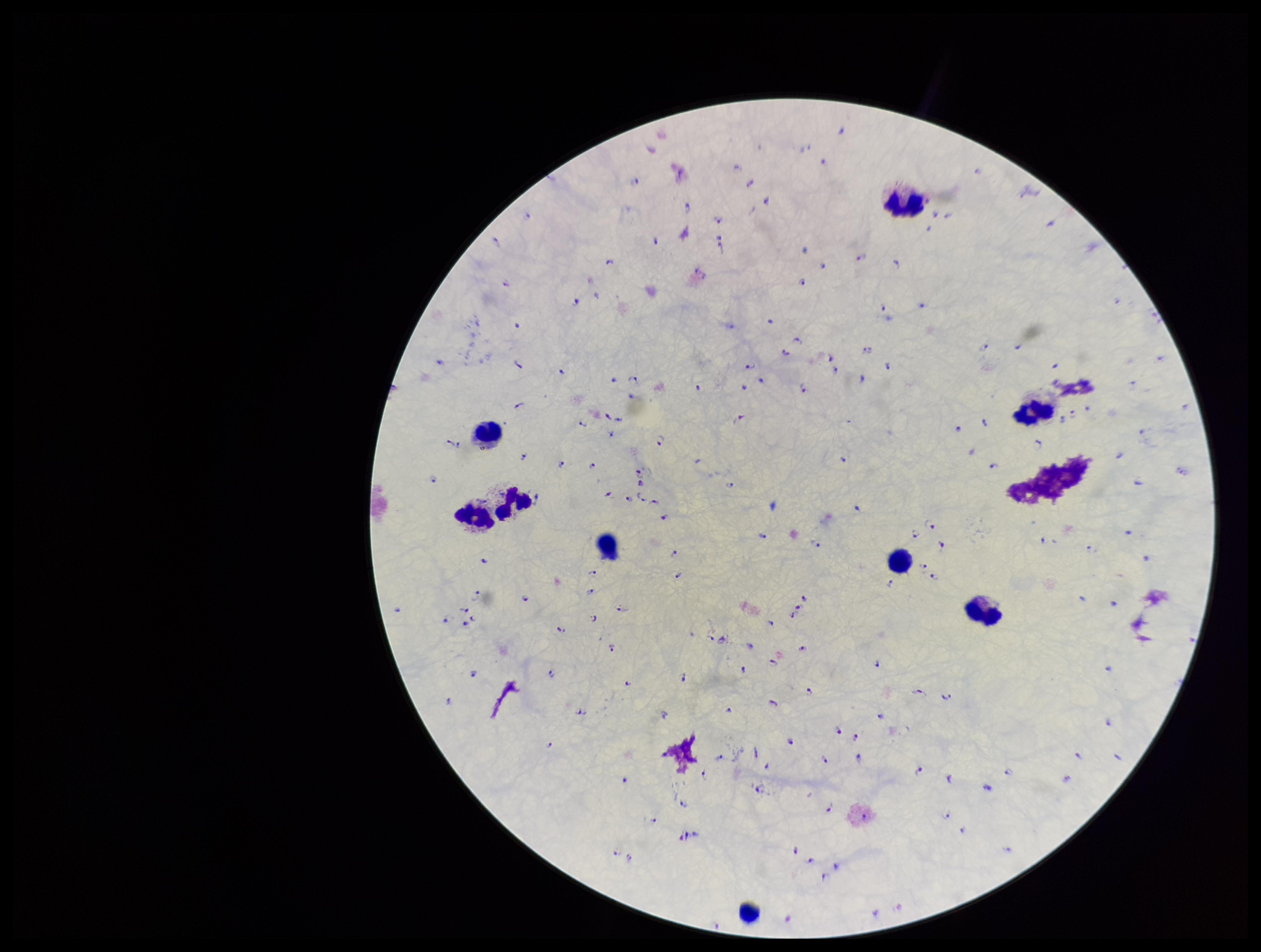

Summary:
  - Plasmodium parasites: detected
  - Patient malaria status: infected
  - Preparation: thick blood smear
  - Species reported for this patient: Plasmodium falciparum
  - Image size: 1261×952 pixels
  - Parasite count: 189
  - Leukocyte count: 9
  - Capture: smartphone photograph through the microscope eyepiece
  - Stain: Giemsa
  - Field of view: single